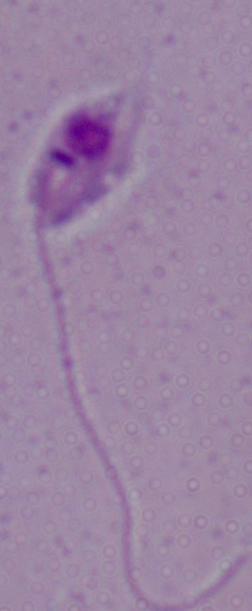
identification = Leishmania
magnification = 1000x
modality = micrograph